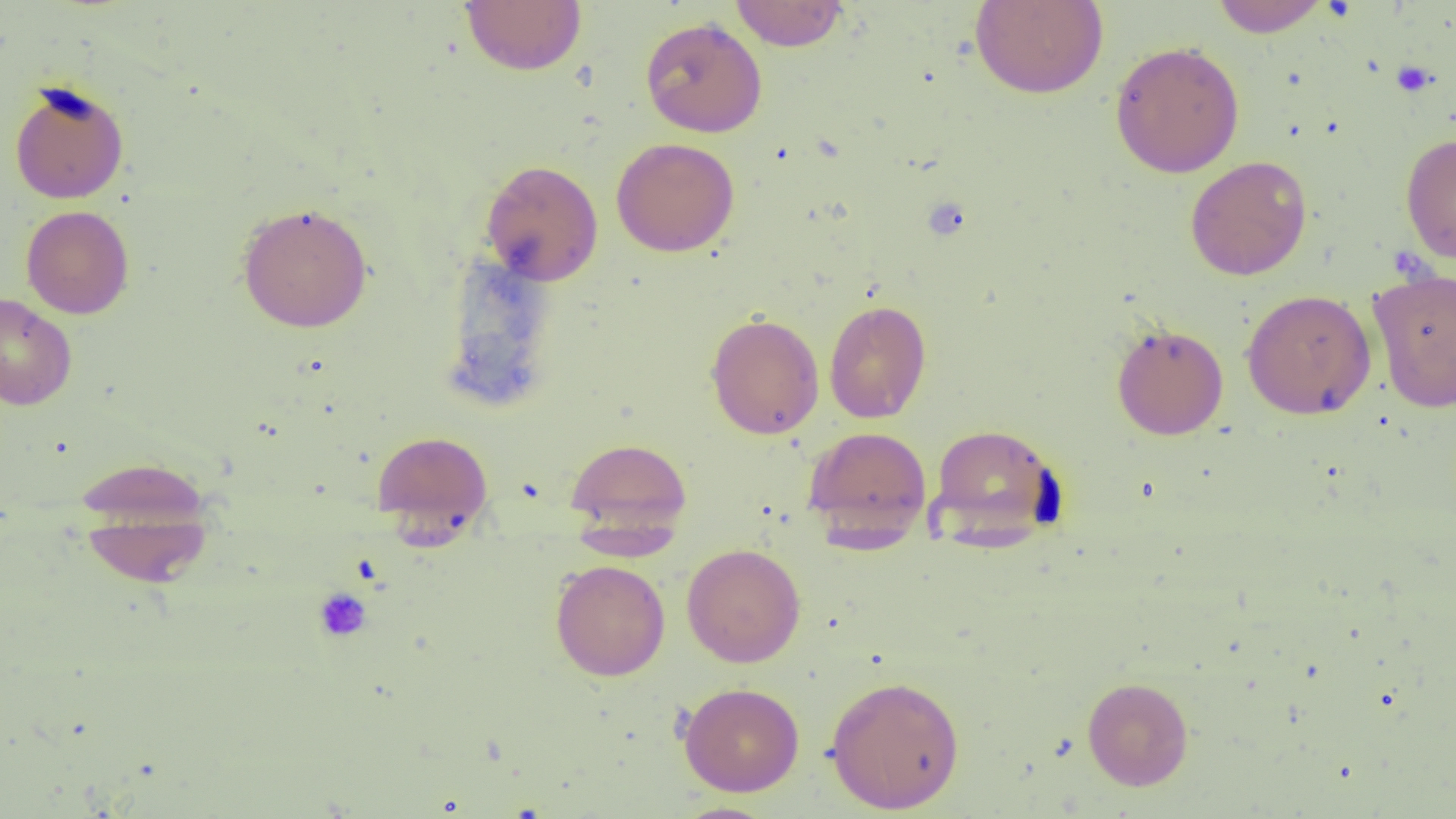

Approximate bounding boxes as (x1,y1)-(x2,y2) corner pairs in pixels. Uninfected red blood cell locations: (460,0)-(587,76), (730,0)-(849,51), (970,0)-(1108,99), (1210,0)-(1331,37), (640,17)-(767,138), (1109,40)-(1245,178), (9,80)-(129,204), (1400,133)-(1456,264), (611,137)-(740,257), (1185,156)-(1312,280), (480,159)-(603,286), (237,202)-(373,332), (21,205)-(134,319), (441,251)-(560,408), (1369,267)-(1456,413), (1242,289)-(1376,418), (0,293)-(77,409), (824,299)-(931,423), (705,312)-(824,439), (1111,323)-(1229,440), (928,424)-(1065,548), (803,426)-(932,544), (371,430)-(493,537), (565,437)-(692,537), (75,453)-(213,552), (78,490)-(214,588), (682,543)-(806,667), (550,559)-(670,681), (825,673)-(965,813), (1082,676)-(1194,790), (679,682)-(805,796), (670,802)-(780,818). Platelet locations: (1391,60)-(1436,96), (313,587)-(372,642). Slide-level diagnosis: no evidence of blood parasites. One field of a larger specimen. Image is 1456×819 pixels. Thin blood smear. Captured at 1000x magnification. Light microscopy.